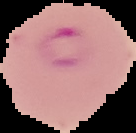
Summary:
  - Preparation: thin blood smear
  - Image type: segmented cell region with the area outside set to black
  - Image size: 136×133 pixels
  - Result: Plasmodium parasites identified